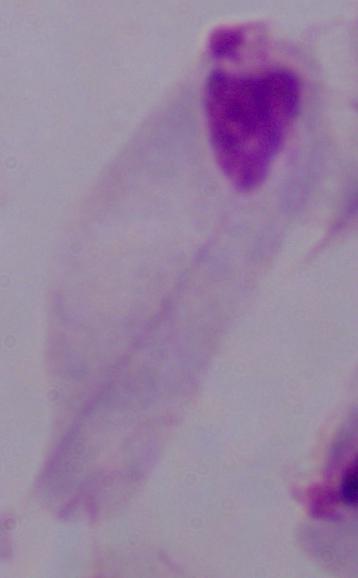
Summary:
  - Identification: trichomonad
  - Modality: micrograph
  - Magnification: 1000x